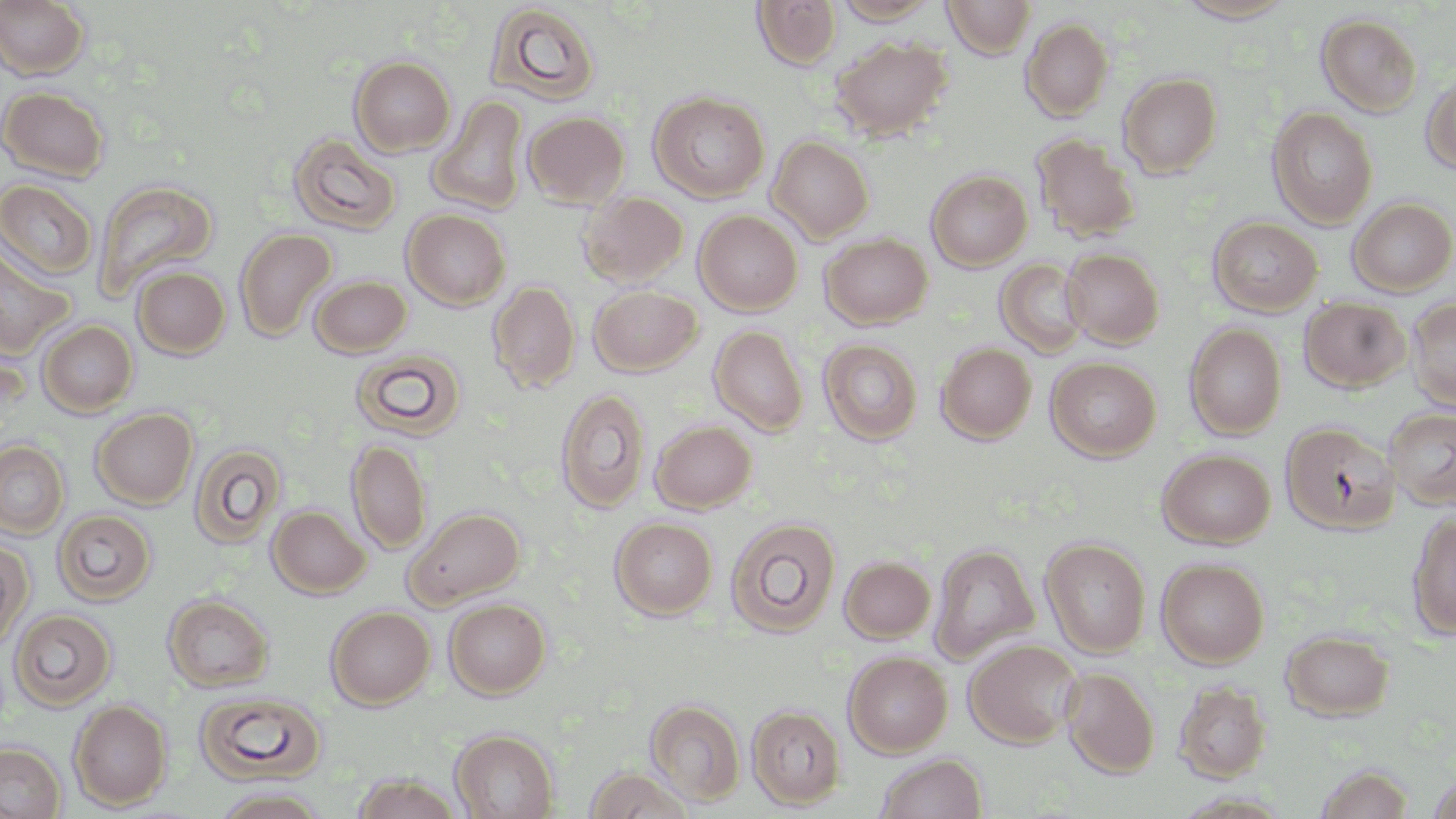
Summary:
  - Coordinate format: approximate bounding boxes as [x1, y1, x2, y2] in pixels
  - Uninfected red blood cell locations: [0, 0, 91, 80], [750, 0, 842, 70], [942, 0, 1036, 60], [1173, 0, 1301, 24], [831, 1, 941, 23], [484, 3, 602, 106], [1316, 13, 1423, 117], [1021, 18, 1113, 121], [828, 36, 953, 142], [349, 56, 455, 156], [1421, 71, 1455, 174], [1118, 72, 1223, 178], [0, 86, 110, 182], [649, 91, 770, 203], [428, 95, 529, 215], [1268, 106, 1378, 228], [522, 110, 630, 209], [287, 133, 401, 235], [1030, 133, 1141, 242], [767, 135, 875, 242], [926, 170, 1032, 271], [0, 179, 98, 280], [93, 179, 219, 300], [579, 190, 688, 287], [1347, 197, 1456, 296], [402, 208, 510, 310], [694, 209, 802, 315], [1208, 216, 1323, 316], [235, 228, 336, 342], [820, 233, 933, 329], [0, 243, 75, 358], [1062, 248, 1164, 348], [996, 258, 1090, 358], [132, 266, 231, 358], [310, 274, 412, 357], [488, 279, 580, 393], [588, 285, 702, 376], [1299, 296, 1412, 392], [1406, 298, 1456, 411], [37, 320, 138, 417], [1185, 323, 1286, 440], [710, 325, 808, 436], [818, 338, 923, 445], [936, 342, 1036, 444], [350, 347, 467, 440], [1046, 357, 1161, 461], [555, 388, 651, 513], [91, 407, 198, 508], [1384, 408, 1456, 509], [650, 420, 757, 513], [1281, 422, 1400, 534], [347, 439, 431, 554], [0, 440, 69, 539], [190, 442, 286, 548], [1158, 449, 1275, 548], [268, 505, 371, 598], [406, 506, 525, 607], [53, 509, 156, 605], [1407, 512, 1456, 640], [610, 517, 718, 619], [726, 517, 841, 637], [1041, 537, 1151, 657], [0, 540, 30, 655], [929, 543, 1039, 662], [840, 555, 936, 643], [1156, 557, 1269, 667], [163, 594, 274, 692], [444, 598, 551, 698], [326, 606, 435, 709], [9, 608, 117, 710], [1282, 630, 1394, 720], [964, 638, 1083, 748], [844, 651, 952, 756], [1061, 667, 1159, 778], [1174, 681, 1272, 782], [195, 691, 327, 784], [645, 698, 746, 806], [69, 699, 172, 810], [746, 705, 845, 809], [450, 729, 559, 819], [0, 740, 66, 819], [874, 753, 988, 818], [1311, 764, 1417, 819], [582, 766, 696, 818], [348, 773, 465, 818], [1426, 775, 1456, 818], [210, 787, 331, 818]
  - Slide-level diagnosis: no evidence of blood parasites
  - Stain: May-Grünwald-Giemsa
  - Modality: light microscopy
  - Preparation: thin blood film
  - Image size: 1456×819 pixels
  - Field of view: single
  - Magnification: 1000x